Comment on the morphology of the red blood cells.
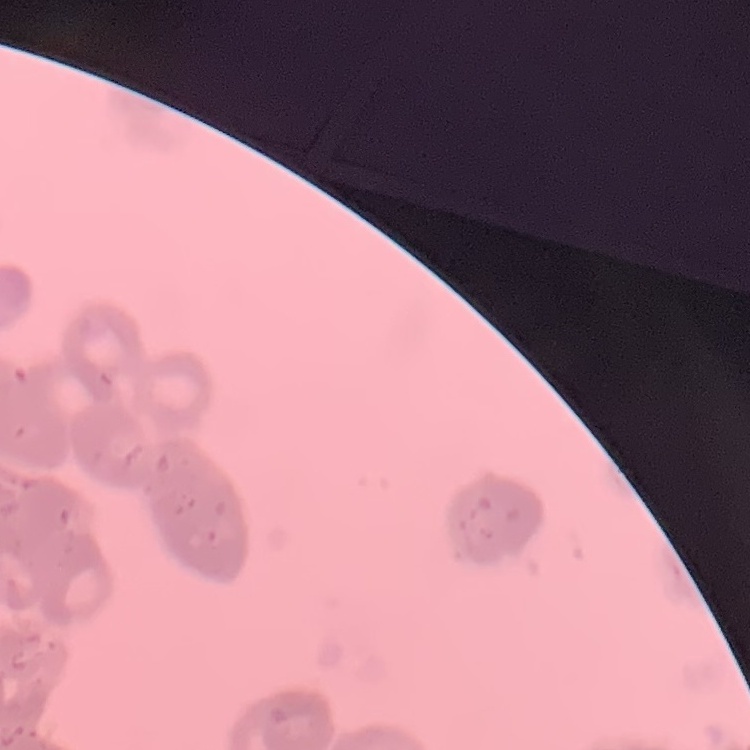

Rouleaux formation.

Thin peripheral smear. One tile cut from a larger photomicrograph. Field's or Giemsa stain.